Give the position of every malaria parasite.
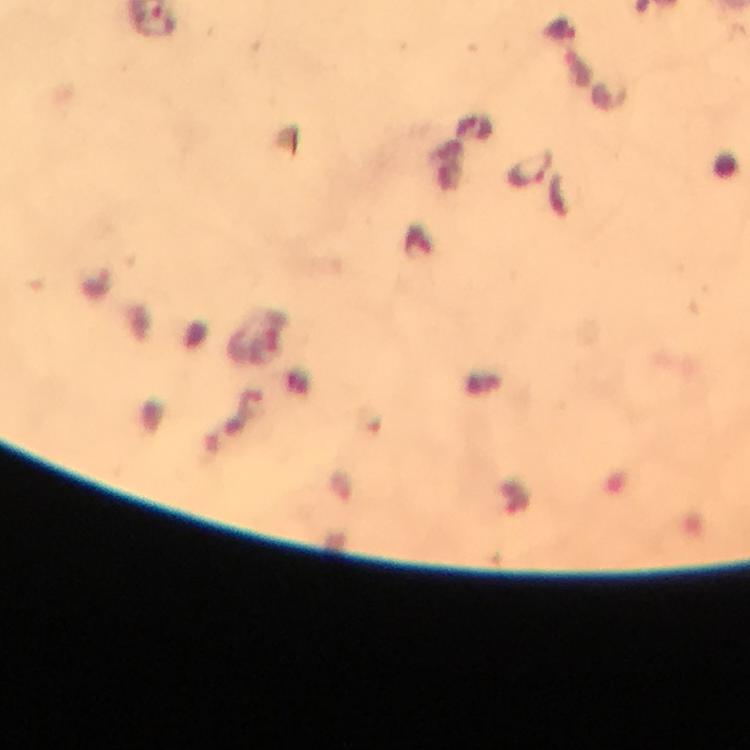
Approximate object centers, in pixels from the top-left corner.
Malaria parasites: (x=529, y=169).

{
  "image_size": "750×750 pixels",
  "capture": "smartphone photograph through a microscope",
  "immersion_oil": "applied",
  "magnification": "100x",
  "context": "from a diagnostic examination for malaria",
  "cropped_from": "one field of view",
  "preparation": "thick blood film",
  "stain": "Giemsa"
}